Classify this cell by malaria status.
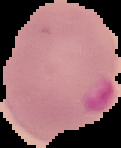

It is parasitized.

Image is 121×148 pixels. Cell region segmented out of the field of view; the surrounding area is masked to black. From a thin blood film.